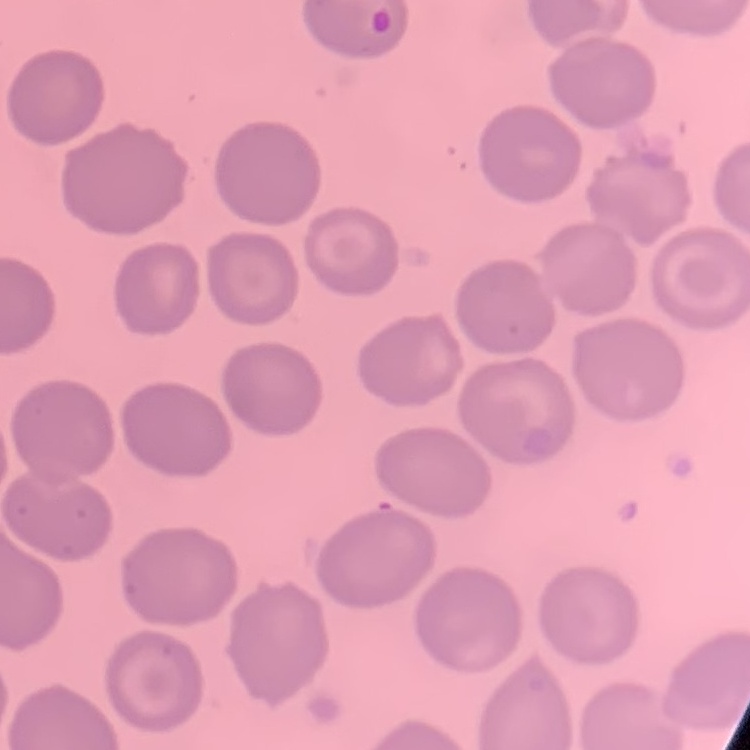
The erythrocytes exhibit no rouleaux formation. Thin blood smear. Square crop of a larger photomicrograph. Stained with either Field's or Giemsa.